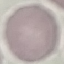
Summary:
  - Result: no malaria parasites detected
  - Stain: Giemsa
  - Image type: automatically extracted cell patch, resized to 64 × 64 pixels
  - Preparation: thin smear
  - Capture: smartphone through the microscope eyepiece